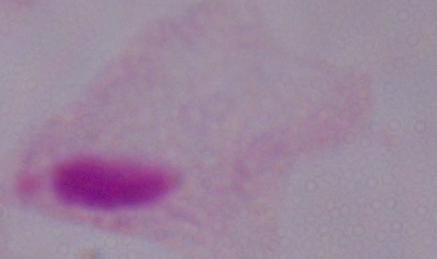
1000x magnification. Photomicrograph. A trichomonad is shown.